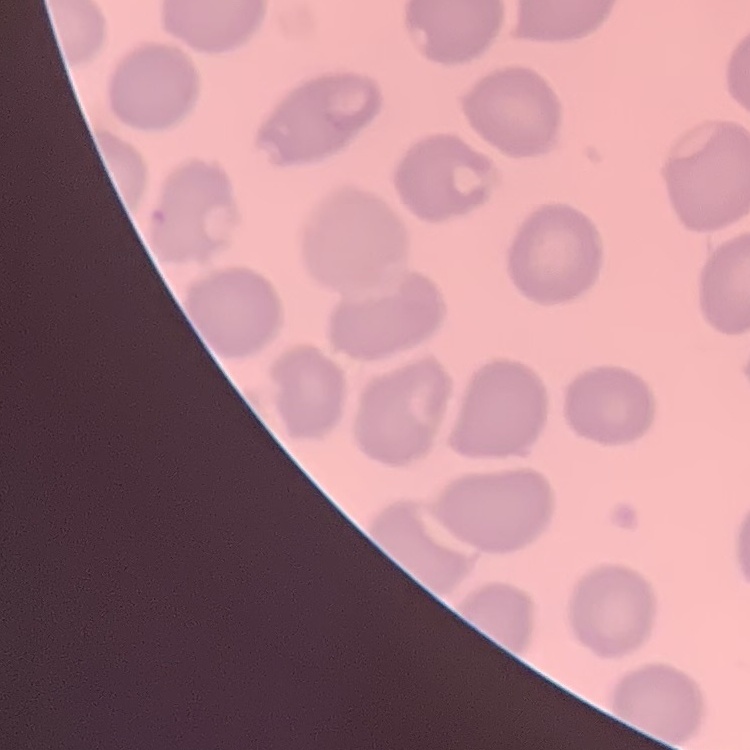
red blood cell morphology = no rouleaux formation
image type = square crop of a larger photomicrograph
preparation = thin blood smear
stain = Field's or Giemsa